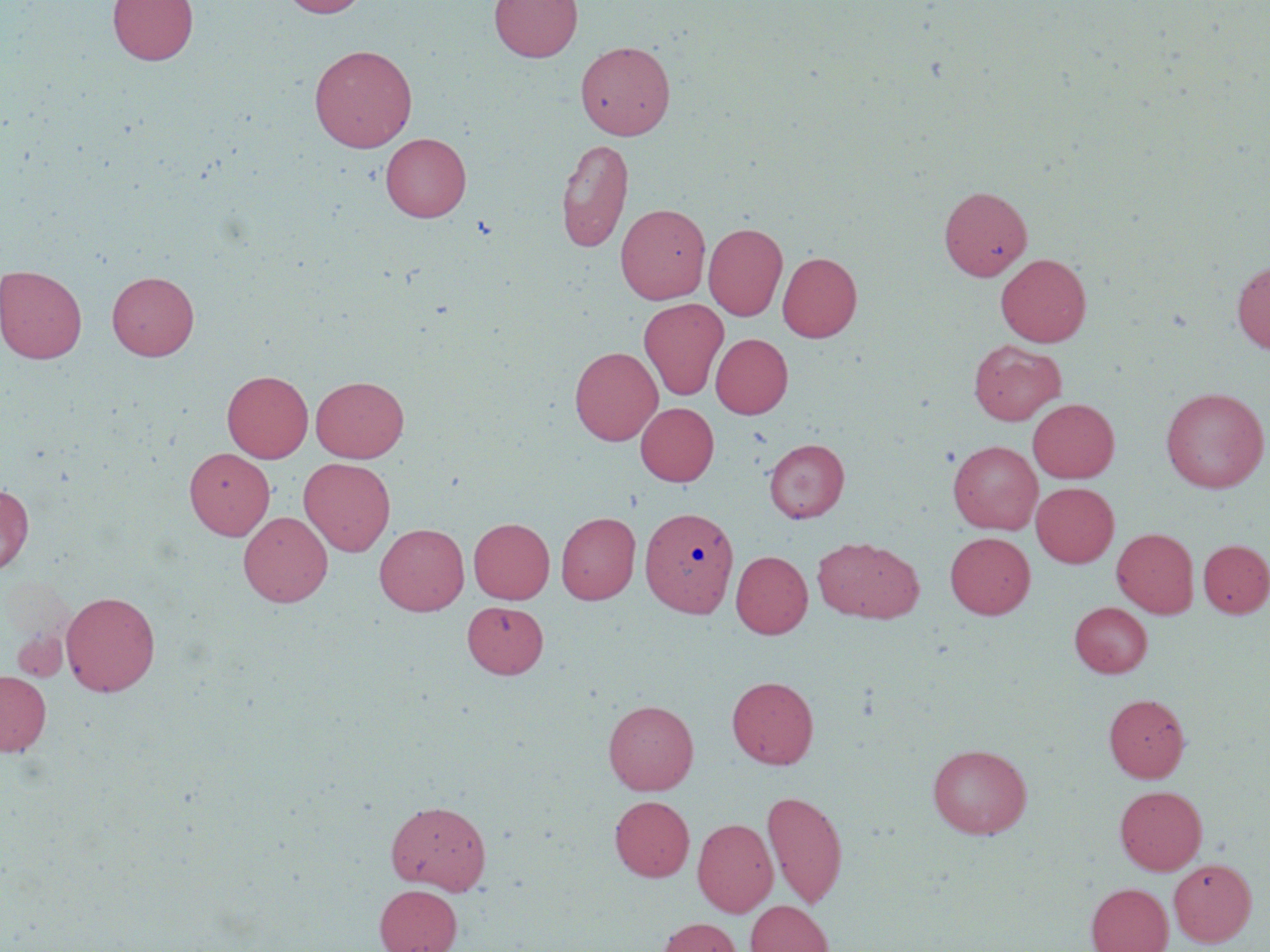
Approximate bounding boxes as named x1/y1/x2/y2 corners in pixels. Uninfected red blood cell locations: (x1=108, y1=0, x2=198, y2=66), (x1=281, y1=0, x2=368, y2=17), (x1=489, y1=0, x2=582, y2=61), (x1=575, y1=40, x2=675, y2=140), (x1=308, y1=44, x2=417, y2=152), (x1=381, y1=133, x2=471, y2=222), (x1=555, y1=137, x2=634, y2=253), (x1=939, y1=185, x2=1032, y2=281), (x1=615, y1=203, x2=711, y2=304), (x1=703, y1=222, x2=787, y2=321), (x1=777, y1=251, x2=862, y2=342), (x1=995, y1=253, x2=1092, y2=347), (x1=1232, y1=260, x2=1270, y2=354), (x1=0, y1=265, x2=87, y2=364), (x1=107, y1=271, x2=199, y2=360), (x1=638, y1=298, x2=729, y2=401), (x1=711, y1=333, x2=793, y2=419), (x1=968, y1=340, x2=1066, y2=425), (x1=570, y1=346, x2=662, y2=445), (x1=222, y1=370, x2=313, y2=463), (x1=311, y1=375, x2=409, y2=463), (x1=1160, y1=387, x2=1268, y2=493), (x1=1028, y1=398, x2=1119, y2=483), (x1=636, y1=402, x2=719, y2=486), (x1=764, y1=438, x2=849, y2=522), (x1=948, y1=440, x2=1042, y2=533), (x1=184, y1=448, x2=274, y2=540), (x1=299, y1=458, x2=395, y2=556), (x1=1031, y1=482, x2=1119, y2=567), (x1=0, y1=483, x2=33, y2=575), (x1=639, y1=506, x2=738, y2=618), (x1=238, y1=511, x2=332, y2=607), (x1=556, y1=512, x2=641, y2=604), (x1=469, y1=517, x2=554, y2=603), (x1=375, y1=523, x2=469, y2=615), (x1=1111, y1=528, x2=1199, y2=618), (x1=945, y1=531, x2=1035, y2=619), (x1=812, y1=536, x2=924, y2=623), (x1=1198, y1=539, x2=1270, y2=618), (x1=731, y1=550, x2=812, y2=639), (x1=60, y1=590, x2=161, y2=696), (x1=462, y1=601, x2=548, y2=678), (x1=1069, y1=602, x2=1152, y2=677), (x1=13, y1=629, x2=67, y2=681), (x1=0, y1=671, x2=51, y2=756), (x1=726, y1=676, x2=819, y2=768), (x1=1104, y1=694, x2=1190, y2=782), (x1=1111, y1=695, x2=1196, y2=874), (x1=603, y1=700, x2=699, y2=795), (x1=927, y1=743, x2=1032, y2=838), (x1=1114, y1=785, x2=1207, y2=874), (x1=762, y1=790, x2=848, y2=909), (x1=609, y1=795, x2=694, y2=882), (x1=386, y1=800, x2=491, y2=894), (x1=693, y1=818, x2=778, y2=916), (x1=1169, y1=858, x2=1256, y2=946), (x1=1085, y1=883, x2=1173, y2=952), (x1=374, y1=885, x2=462, y2=952), (x1=745, y1=900, x2=834, y2=952), (x1=654, y1=917, x2=744, y2=952). Slide-level diagnosis: no evidence of blood parasites. Captured at 1000x magnification. Image is 1270×952 pixels. Thin blood film. May-Grünwald-Giemsa-stained preparation. Light microscopy. Single field of view.